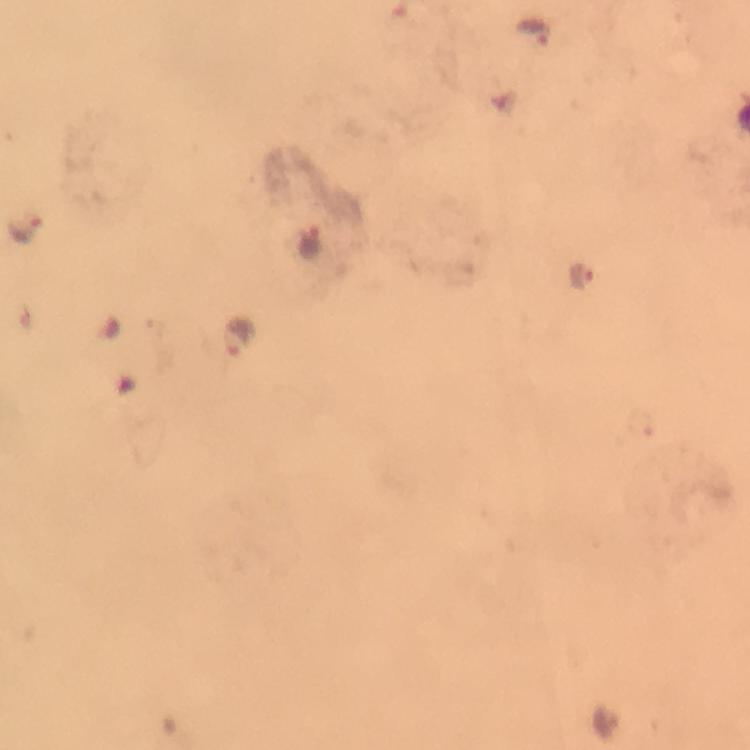

Approximate centers as [x, y] in pixels.
Summary:
  - Malaria parasite locations: [536, 31], [25, 225], [308, 241], [580, 278], [239, 336]
  - Cropped from: a single field of view
  - Magnification: 100x
  - Image size: 750×750 pixels
  - Stain: Giemsa
  - Capture: smartphone camera through the microscope
  - Immersion oil: applied
  - Context: from a diagnostic examination for malaria
  - Preparation: thick smear